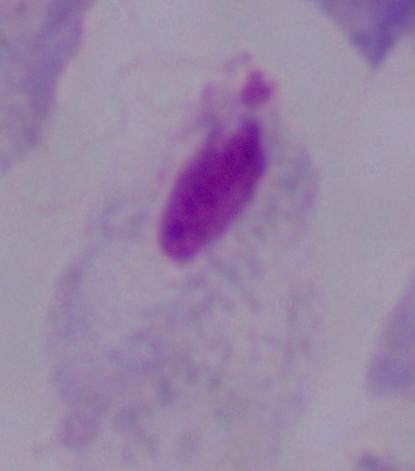

1000x magnification. A trichomonad is shown. Micrograph.